Describe the morphology of the red blood cells.
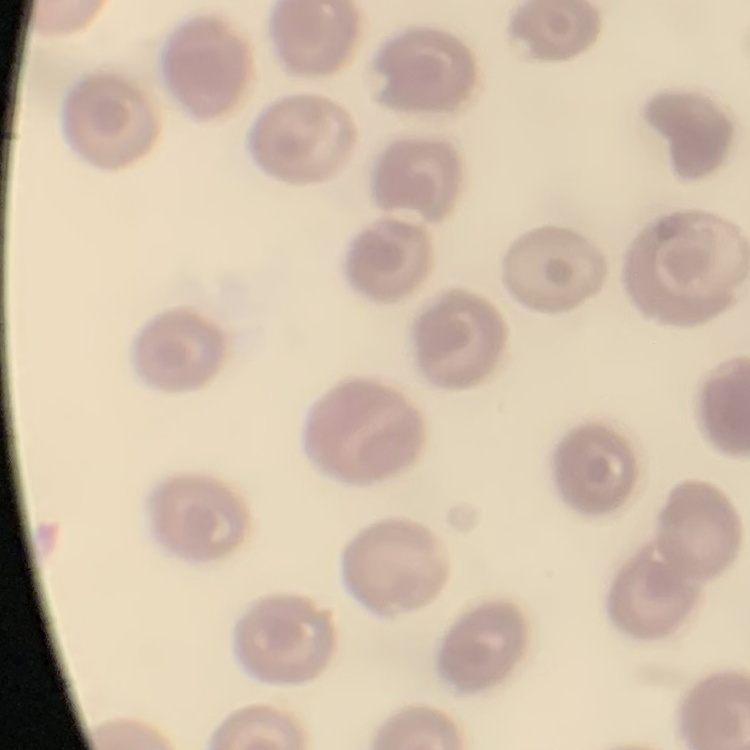

No rouleaux formation.

Thin blood film. Field's or Giemsa stain. One tile cut from a larger photomicrograph.